Identify the blood parasite species.
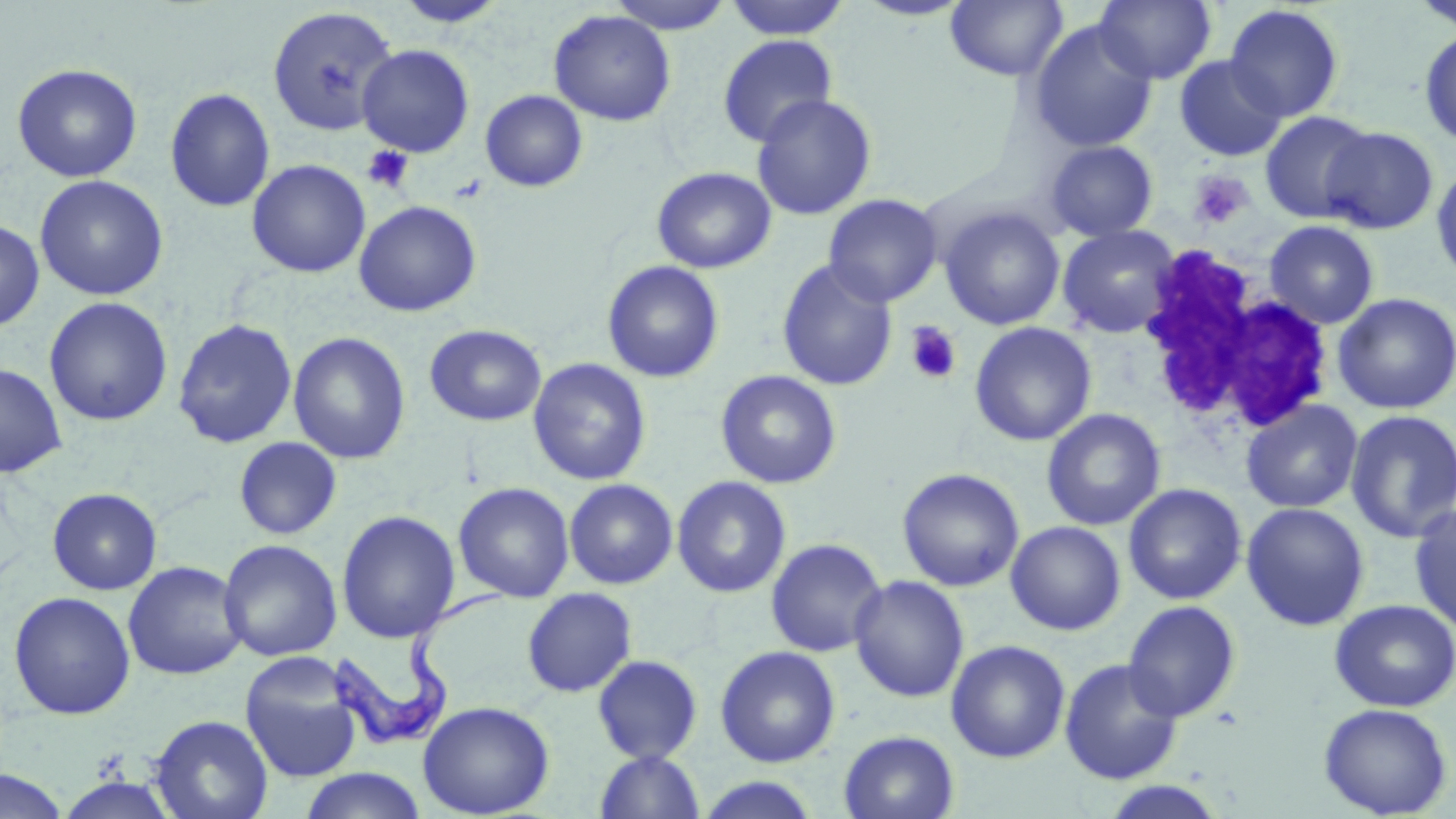
Trypanosoma brucei.

Summary:
  - Coordinate format: approximate bounding boxes as named x1/y1/x2/y2 corners in pixels
  - Trypanosoma brucei locations: (x1=324, y1=583, x2=505, y2=748)
  - White blood cell locations: (x1=1131, y1=243, x2=1333, y2=440)
  - Platelet locations: (x1=362, y1=145, x2=414, y2=194), (x1=1188, y1=170, x2=1253, y2=230), (x1=448, y1=174, x2=489, y2=203), (x1=905, y1=321, x2=963, y2=386)
  - Uninfected red blood cell locations: (x1=606, y1=0, x2=736, y2=34), (x1=723, y1=0, x2=852, y2=40), (x1=854, y1=0, x2=974, y2=21), (x1=1094, y1=0, x2=1216, y2=85), (x1=1411, y1=0, x2=1456, y2=32), (x1=393, y1=1, x2=509, y2=28), (x1=945, y1=1, x2=1068, y2=82), (x1=1224, y1=4, x2=1344, y2=122), (x1=267, y1=6, x2=398, y2=137), (x1=548, y1=10, x2=677, y2=127), (x1=1028, y1=20, x2=1158, y2=153), (x1=1418, y1=28, x2=1456, y2=149), (x1=718, y1=35, x2=838, y2=148), (x1=356, y1=44, x2=474, y2=157), (x1=1173, y1=55, x2=1287, y2=162), (x1=11, y1=62, x2=142, y2=182), (x1=165, y1=87, x2=276, y2=213), (x1=480, y1=90, x2=588, y2=193), (x1=751, y1=94, x2=877, y2=221), (x1=1260, y1=109, x2=1375, y2=224), (x1=1320, y1=126, x2=1439, y2=234), (x1=1044, y1=140, x2=1158, y2=242), (x1=247, y1=159, x2=371, y2=278), (x1=1431, y1=161, x2=1456, y2=284), (x1=652, y1=166, x2=776, y2=274), (x1=34, y1=174, x2=168, y2=301), (x1=823, y1=193, x2=942, y2=307), (x1=354, y1=200, x2=481, y2=317), (x1=939, y1=206, x2=1065, y2=331), (x1=0, y1=219, x2=45, y2=332), (x1=1264, y1=220, x2=1380, y2=329), (x1=1057, y1=224, x2=1181, y2=339), (x1=777, y1=259, x2=898, y2=392), (x1=602, y1=260, x2=725, y2=383), (x1=1332, y1=292, x2=1455, y2=414), (x1=43, y1=297, x2=173, y2=427), (x1=172, y1=318, x2=298, y2=449), (x1=969, y1=322, x2=1097, y2=446), (x1=424, y1=324, x2=547, y2=427), (x1=288, y1=332, x2=411, y2=464), (x1=527, y1=358, x2=652, y2=486), (x1=0, y1=362, x2=67, y2=478), (x1=715, y1=369, x2=842, y2=489), (x1=1240, y1=399, x2=1363, y2=513), (x1=1041, y1=408, x2=1166, y2=531), (x1=1345, y1=409, x2=1456, y2=543), (x1=234, y1=436, x2=342, y2=540), (x1=897, y1=467, x2=1024, y2=592), (x1=672, y1=476, x2=792, y2=598), (x1=564, y1=478, x2=678, y2=589), (x1=453, y1=482, x2=575, y2=603), (x1=1123, y1=483, x2=1247, y2=605), (x1=47, y1=487, x2=162, y2=595), (x1=1241, y1=502, x2=1369, y2=631), (x1=1409, y1=504, x2=1456, y2=634), (x1=336, y1=510, x2=459, y2=643), (x1=1006, y1=521, x2=1126, y2=635), (x1=765, y1=537, x2=887, y2=657), (x1=218, y1=539, x2=342, y2=662), (x1=122, y1=561, x2=248, y2=680), (x1=849, y1=575, x2=969, y2=703), (x1=521, y1=587, x2=638, y2=698), (x1=8, y1=591, x2=135, y2=720), (x1=1329, y1=599, x2=1456, y2=712), (x1=1123, y1=600, x2=1241, y2=722), (x1=946, y1=640, x2=1071, y2=763), (x1=715, y1=645, x2=841, y2=767), (x1=239, y1=653, x2=364, y2=783), (x1=592, y1=654, x2=704, y2=764), (x1=1059, y1=658, x2=1184, y2=784), (x1=417, y1=700, x2=555, y2=817), (x1=1318, y1=702, x2=1452, y2=818), (x1=150, y1=714, x2=273, y2=819), (x1=838, y1=730, x2=960, y2=819), (x1=594, y1=750, x2=706, y2=818), (x1=299, y1=768, x2=427, y2=819), (x1=0, y1=769, x2=70, y2=818), (x1=54, y1=774, x2=179, y2=818), (x1=694, y1=775, x2=823, y2=818), (x1=1099, y1=780, x2=1227, y2=819)
  - Field of view: single
  - Stain: May-Grünwald-Giemsa
  - Preparation: thin blood smear
  - Image size: 1456×819 pixels
  - Modality: light microscopy
  - Magnification: 1000x